Classify this cell by malaria status.
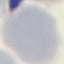
It is uninfected.

Summary:
  - Stain: Giemsa
  - Capture: smartphone camera at the microscope eyepiece
  - Preparation: thin smear
  - Image type: automatically extracted cell patch, resized to 64 × 64 pixels